Locate every Plasmodium falciparum-infected red blood cell.
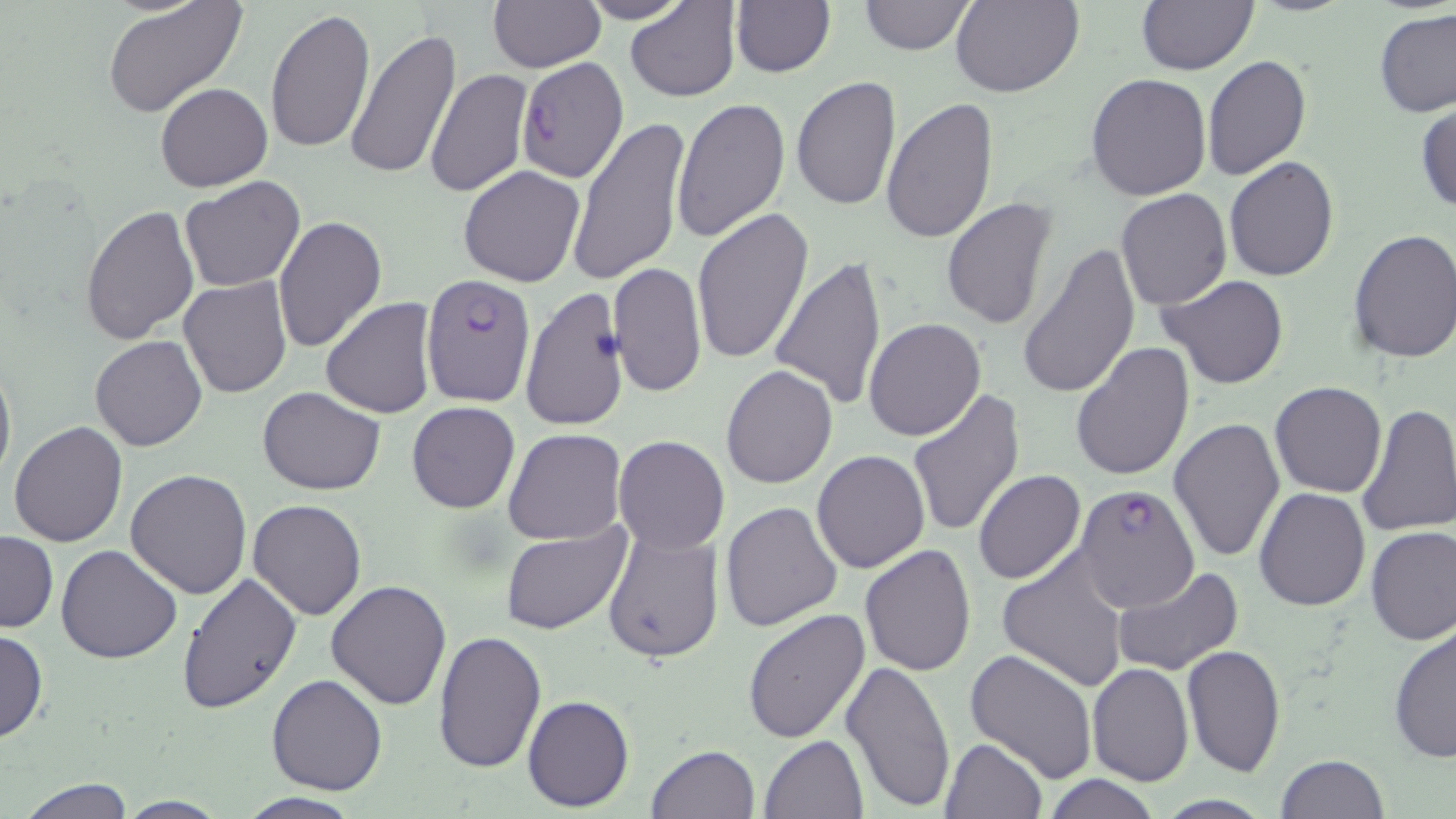
Approximate bounding boxes as (x1,y1)-(x2,y2) corner pairs in pixels.
Plasmodium falciparum-infected red blood cells: (511,57)-(631,187), (421,274)-(537,406), (1071,491)-(1207,622).

Summary:
  - Uninfected red blood cell locations: (104,0)-(246,118), (575,0)-(694,24), (625,0)-(742,102), (729,0)-(835,78), (950,0)-(1083,98), (1135,0)-(1258,75), (487,1)-(605,72), (856,1)-(977,55), (265,9)-(374,155), (1376,9)-(1456,118), (344,27)-(461,181), (1202,56)-(1311,180), (425,66)-(533,199), (1085,73)-(1212,202), (790,75)-(902,212), (156,82)-(274,193), (671,96)-(791,245), (881,97)-(1000,245), (1416,104)-(1456,216), (568,116)-(690,288), (1224,158)-(1339,281), (458,165)-(586,287), (180,176)-(306,291), (1115,189)-(1232,310), (941,197)-(1058,330), (80,203)-(199,345), (690,207)-(813,367), (272,214)-(387,354), (1347,230)-(1456,363), (1019,243)-(1141,398), (771,256)-(888,409), (609,261)-(707,401), (1160,275)-(1290,390), (179,276)-(292,398), (519,285)-(628,432), (321,299)-(436,419), (864,318)-(985,439), (90,335)-(207,451), (1070,342)-(1195,482), (0,356)-(16,493), (721,365)-(839,489), (1269,382)-(1388,498), (258,387)-(384,494), (906,387)-(1025,539), (406,402)-(520,513), (1358,402)-(1456,537), (1168,417)-(1286,562), (7,422)-(128,546), (503,429)-(626,544), (612,435)-(729,554), (811,449)-(930,574), (125,468)-(251,598), (972,469)-(1086,584), (1255,486)-(1370,612), (246,498)-(365,620), (720,501)-(842,632), (501,525)-(632,636), (602,525)-(724,664), (1366,525)-(1456,644), (1,530)-(57,633), (860,543)-(977,676), (56,545)-(182,664), (996,550)-(1130,691), (1111,565)-(1243,677), (177,574)-(302,713), (326,579)-(452,710), (1138,590)-(1276,735), (743,607)-(871,745), (1389,621)-(1456,764), (0,629)-(48,743), (433,630)-(547,773), (1181,644)-(1287,777), (964,646)-(1097,783), (442,653)-(617,796), (840,659)-(956,811), (1086,663)-(1193,785), (267,673)-(388,795), (524,695)-(635,811), (760,734)-(868,819), (938,737)-(1049,819), (645,744)-(761,819), (1276,754)-(1388,819), (1044,776)-(1161,818), (15,778)-(136,818), (234,792)-(364,818), (115,798)-(231,818)
  - Slide-level diagnosis: Plasmodium falciparum
  - Modality: optical microscopy
  - Image size: 1456×819 pixels
  - Preparation: thin blood smear
  - Stain: May-Grünwald-Giemsa
  - Magnification: 1000x
  - Field of view: single